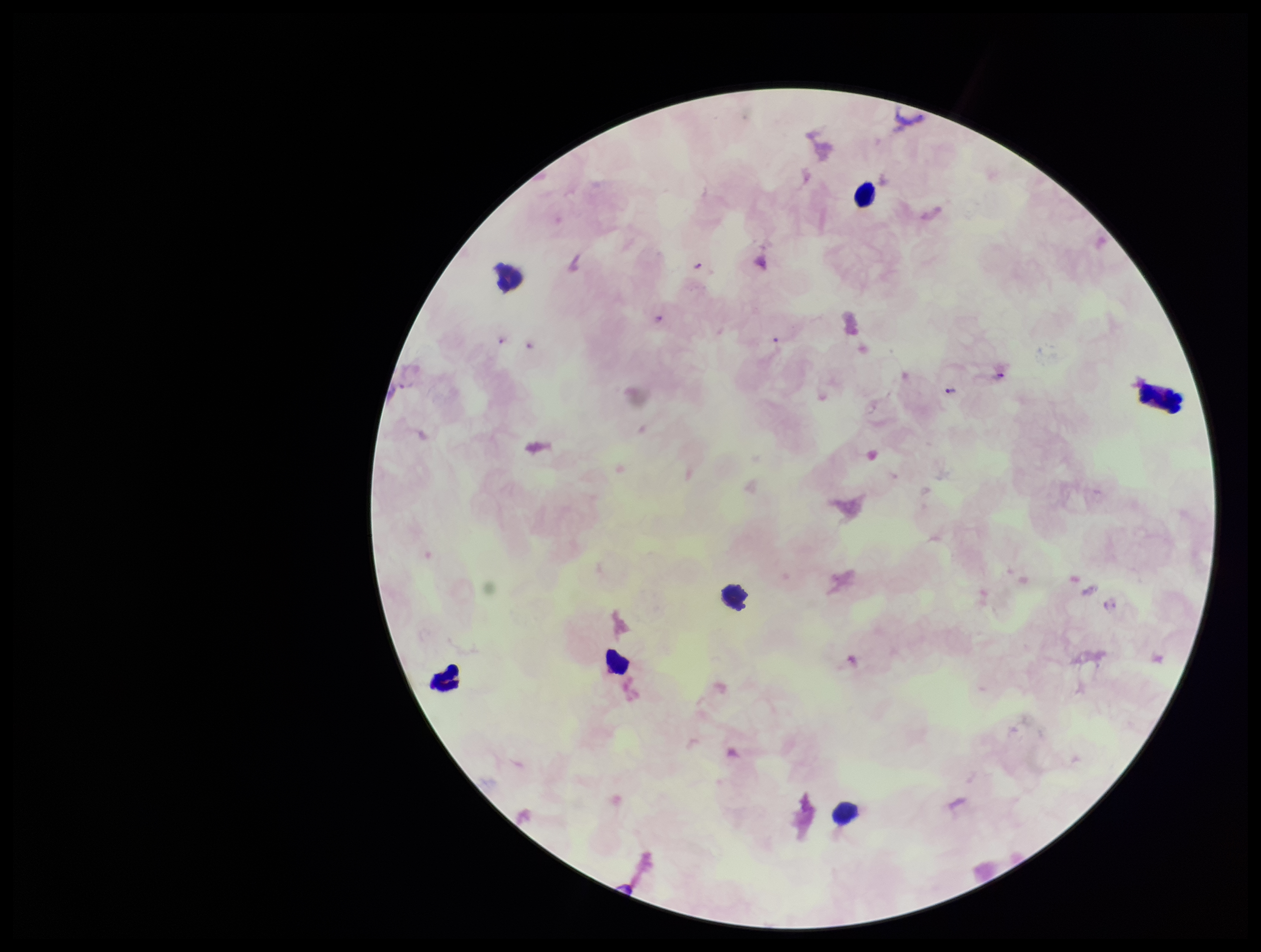
Summary:
  - Capture: smartphone photograph through the microscope eyepiece
  - Species reported for this patient: Plasmodium falciparum
  - Leukocyte count: 5
  - Plasmodium parasites: seen
  - Stain: Giemsa
  - Patient malaria status: infected
  - Preparation: thick smear
  - Parasite count: 7
  - Image size: 1261×952 pixels
  - Field of view: one from this slide